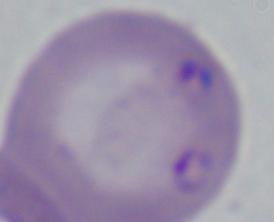 A Babesia parasite is seen. Photomicrograph. 1000x magnification.